Report the malaria status of this cell.
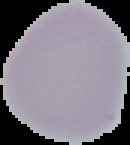

Uninfected.

From a thin blood film. Image is 130×145 pixels. The area outside the segmented cell region is set to black.